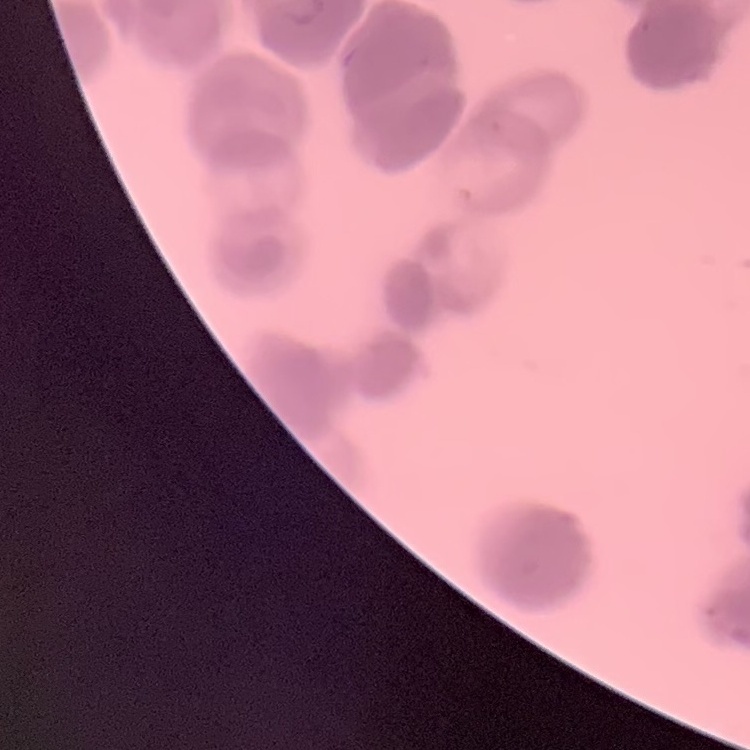
Summary:
  - Erythrocyte morphology: rouleaux formation
  - Image type: one tile cut from a larger photomicrograph
  - Stain: Field's or Giemsa
  - Preparation: thin peripheral smear